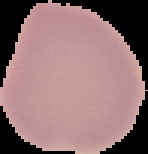
Summary:
  - Image size: 148×154 pixels
  - Preparation: thin blood film
  - Malaria status: uninfected
  - Image type: segmented cell region on a black background